Name the parasite shown.
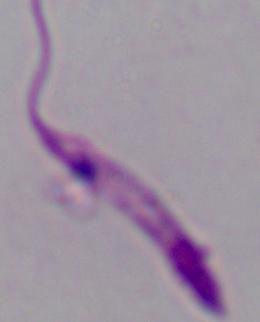

Leishmania.

Micrograph. Captured at 1000x magnification.